State which parasite is depicted.
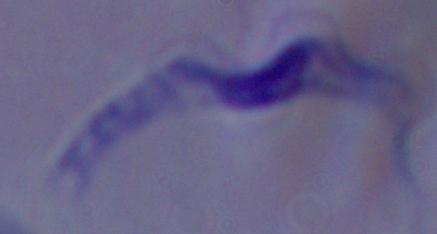

This is a trypanosome.

Captured at 1000x magnification. Micrograph.